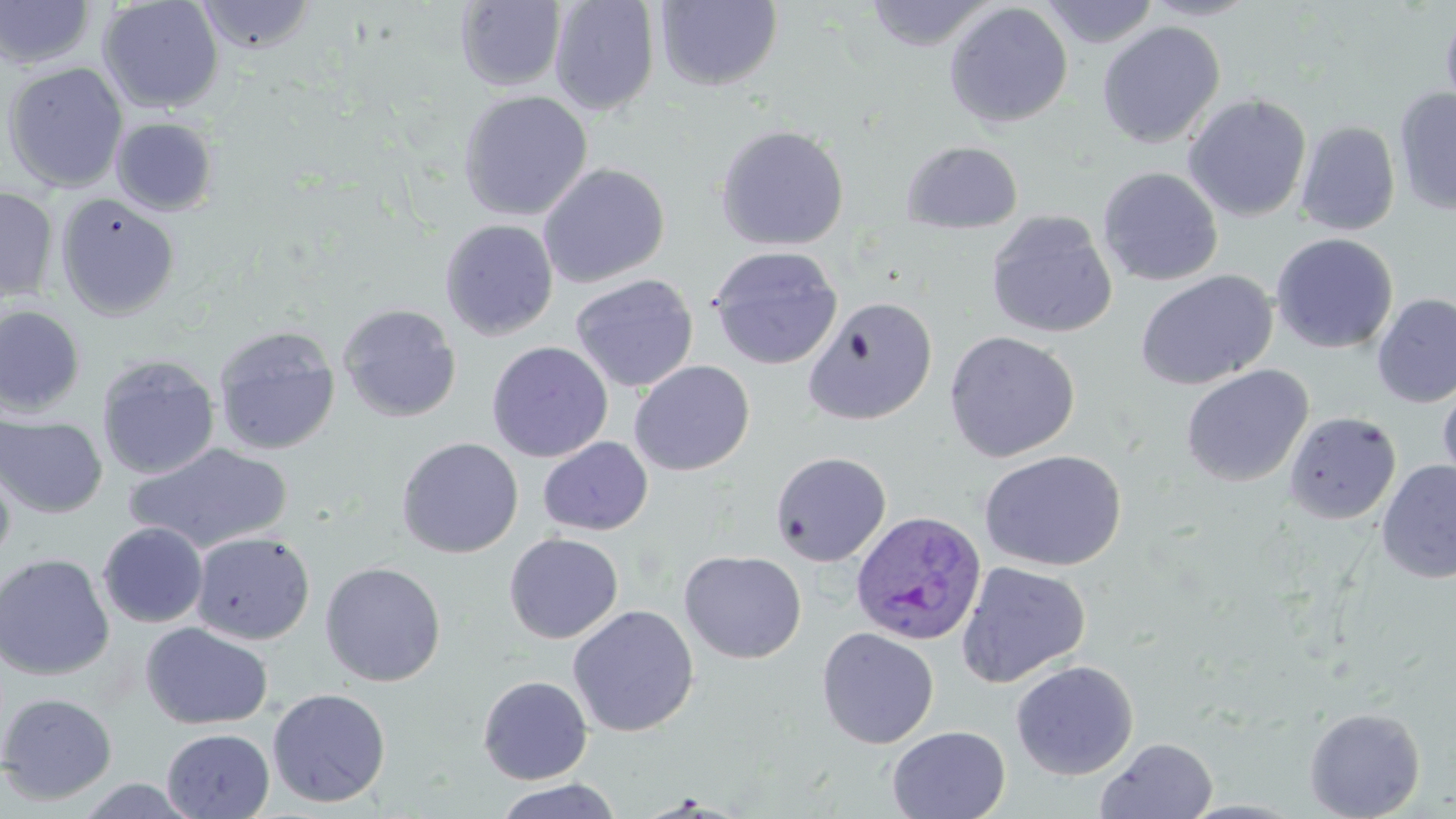
Approximate bounding boxes as [x1, y1, x2, y2] in pixels. Plasmodium ovale-infected red blood cell locations: [851, 509, 988, 648]. Uninfected red blood cell locations: [0, 0, 96, 69], [98, 0, 224, 114], [549, 0, 660, 115], [655, 0, 783, 91], [864, 0, 996, 50], [1041, 0, 1160, 48], [1139, 0, 1264, 21], [195, 1, 317, 54], [456, 1, 567, 91], [944, 2, 1073, 129], [1440, 5, 1456, 127], [1097, 21, 1225, 148], [3, 62, 129, 193], [1394, 88, 1456, 216], [458, 90, 593, 221], [1182, 93, 1312, 222], [112, 117, 219, 216], [1296, 121, 1400, 236], [714, 124, 850, 251], [901, 140, 1023, 234], [537, 163, 670, 288], [1098, 167, 1223, 287], [0, 186, 59, 303], [55, 193, 180, 320], [984, 210, 1118, 338], [439, 219, 559, 341], [1271, 233, 1398, 354], [708, 245, 843, 370], [1135, 270, 1277, 390], [570, 273, 699, 393], [1372, 293, 1456, 408], [802, 295, 938, 425], [338, 303, 461, 422], [0, 305, 86, 417], [213, 325, 340, 456], [944, 330, 1081, 463], [486, 341, 613, 462], [96, 355, 220, 480], [629, 360, 755, 476], [1181, 365, 1313, 487], [1438, 381, 1456, 491], [1283, 411, 1401, 525], [0, 414, 108, 519], [538, 436, 653, 536], [396, 437, 524, 558], [125, 442, 293, 554], [979, 450, 1126, 572], [770, 451, 891, 567], [0, 455, 16, 570], [1376, 460, 1456, 584], [97, 522, 208, 628], [191, 531, 315, 645], [504, 533, 624, 644], [679, 550, 807, 664], [0, 553, 115, 680], [319, 561, 446, 687], [956, 561, 1091, 687], [567, 604, 700, 736], [140, 622, 273, 730], [816, 627, 939, 749], [1010, 660, 1139, 780], [478, 675, 593, 784], [267, 687, 391, 808], [0, 692, 117, 805], [1304, 706, 1426, 819], [887, 725, 1010, 819], [162, 728, 274, 818], [1095, 737, 1218, 819], [74, 776, 201, 819], [492, 778, 622, 819]. Slide-level diagnosis: Plasmodium ovale. 1000x magnification. May-Grünwald-Giemsa-stained preparation. One field of a larger specimen. Thin blood film. Light microscopy. Image is 1456×819 pixels.